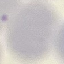

Malaria status: uninfected. Photographed with a smartphone camera at the microscope eyepiece. Giemsa stain. Thin blood smear. Cell patch, automatically extracted from a larger field of view and resized to 64 × 64 pixels.